Describe the morphology of the red blood cells.
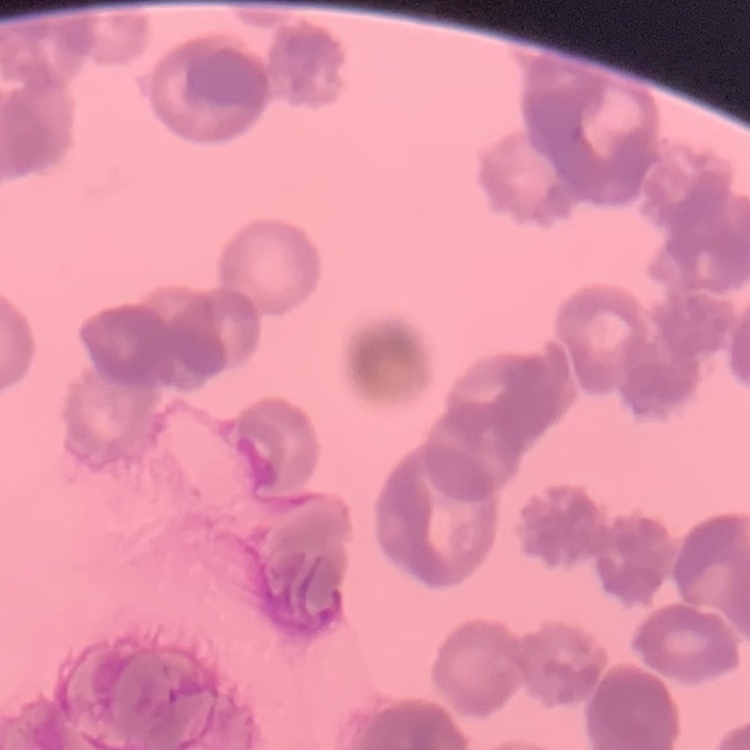

They show rouleaux formation.

Summary:
  - Image type: square crop of a larger photomicrograph
  - Preparation: thin blood smear
  - Stain: Field's or Giemsa